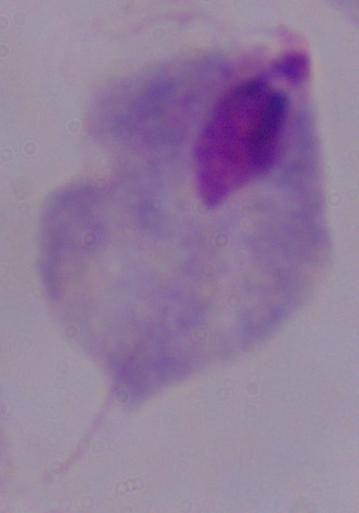

Summary:
  - Magnification: 1000x
  - Modality: micrograph
  - Identification: trichomonad